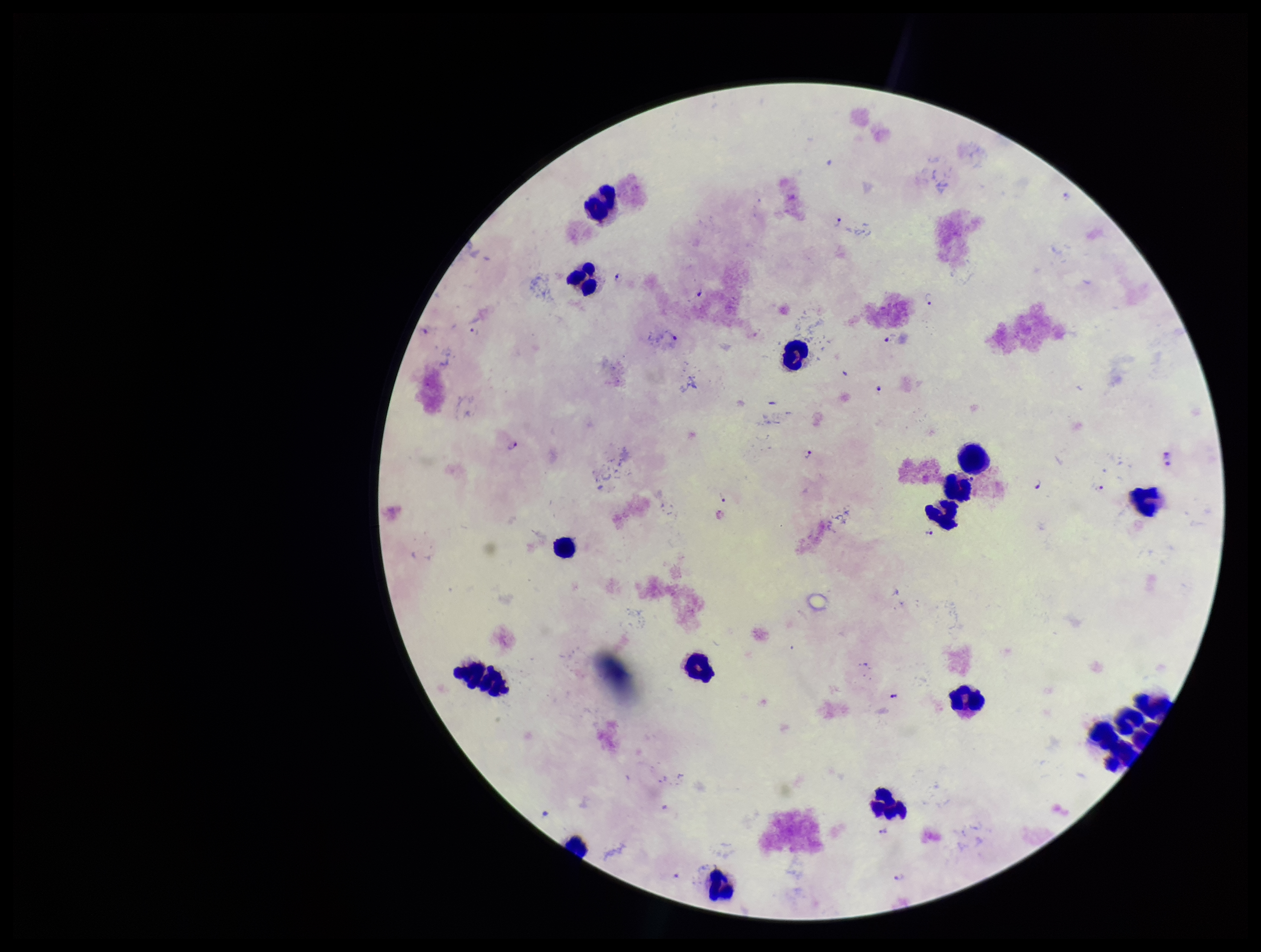
image size = 1261×952 pixels
capture = smartphone photograph through the microscope eyepiece
Plasmodium parasites = detected
preparation = thick smear
leukocyte count = 17
stain = Giemsa
species reported for this patient = Plasmodium falciparum
parasite count = 12
patient malaria status = infected
field of view = one from this slide